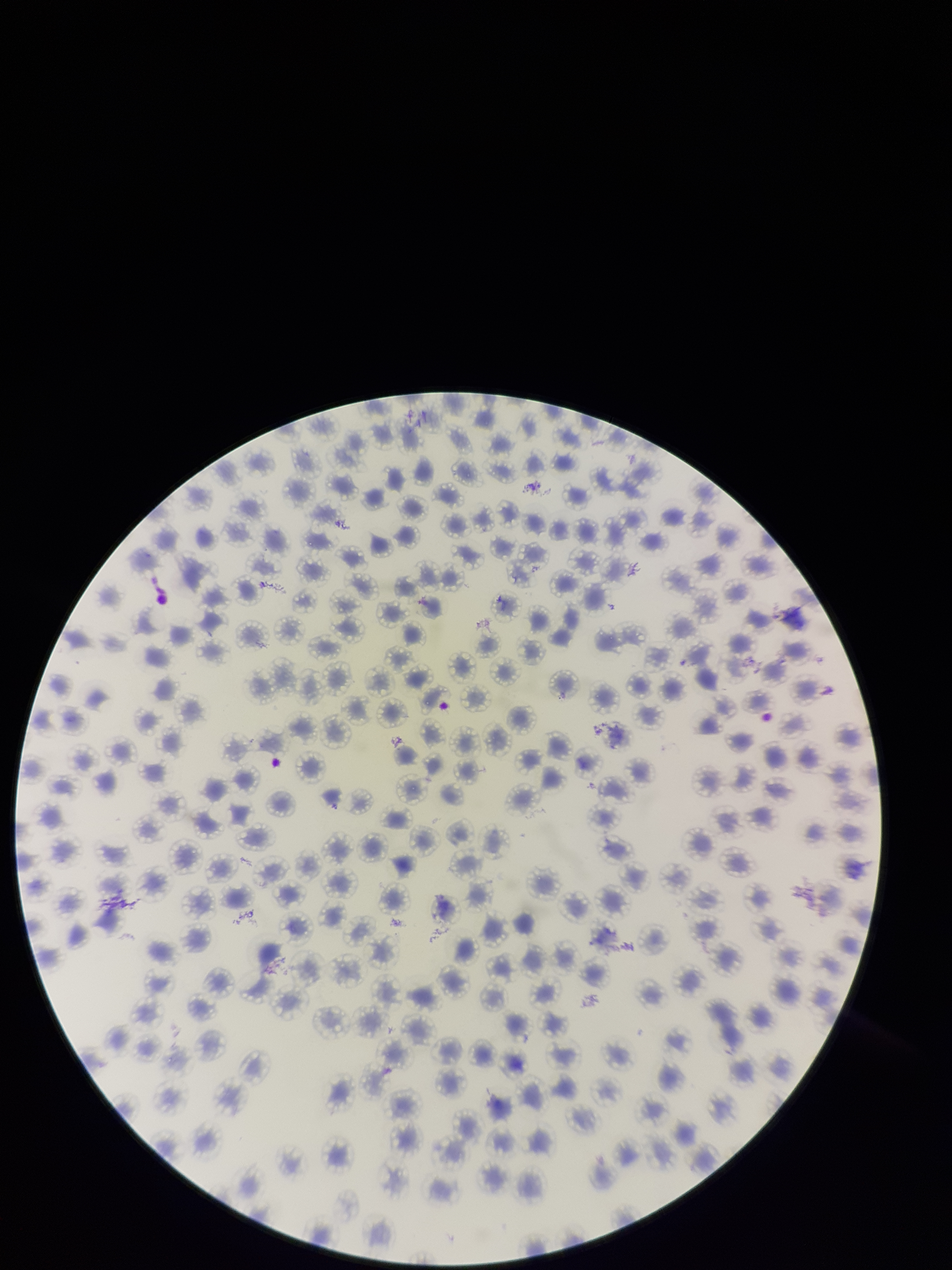
stain = Giemsa
field of view = single
red blood cell count = 149
species reported for this patient = Plasmodium falciparum
patient malaria status = positive
parasitized red blood cell count = 0
capture = smartphone photograph through the microscope eyepiece
preparation = thin
image size = 952×1270 pixels
parasitized red blood cells = none identified